Report the malaria status of this cell.
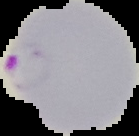

It is parasitized.

{
  "image_size": "139×136 pixels",
  "image_type": "cell region segmented out of the field of view; surrounding area masked to black",
  "preparation": "thin blood smear"
}